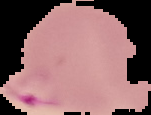

Summary:
  - Preparation: thin blood smear
  - Image size: 151×115 pixels
  - Malaria status: parasitized
  - Image type: segmented cell region on a black background